Describe the morphology of the erythrocytes.
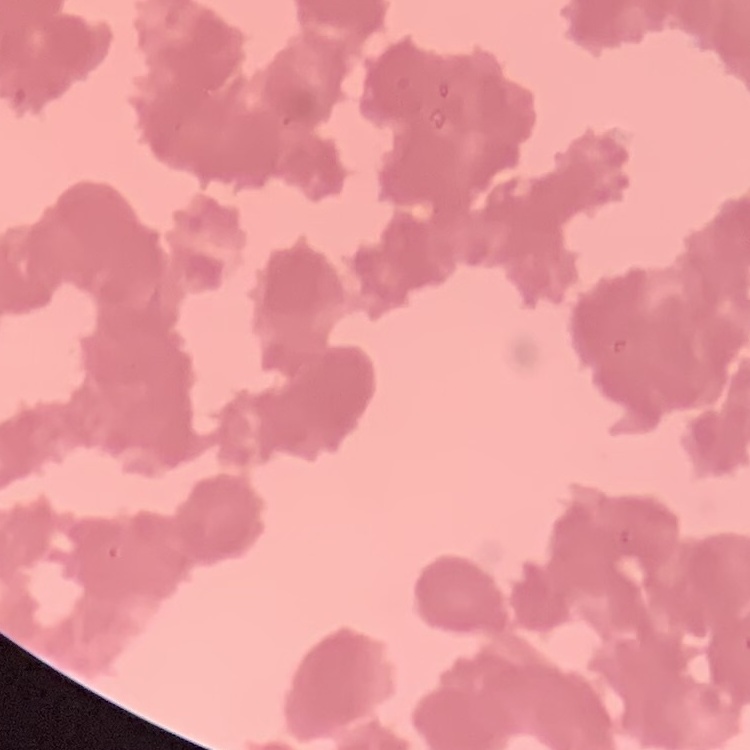
They show rouleaux formation.

stain = Field's or Giemsa
preparation = thin peripheral smear
image type = square crop of a larger photomicrograph